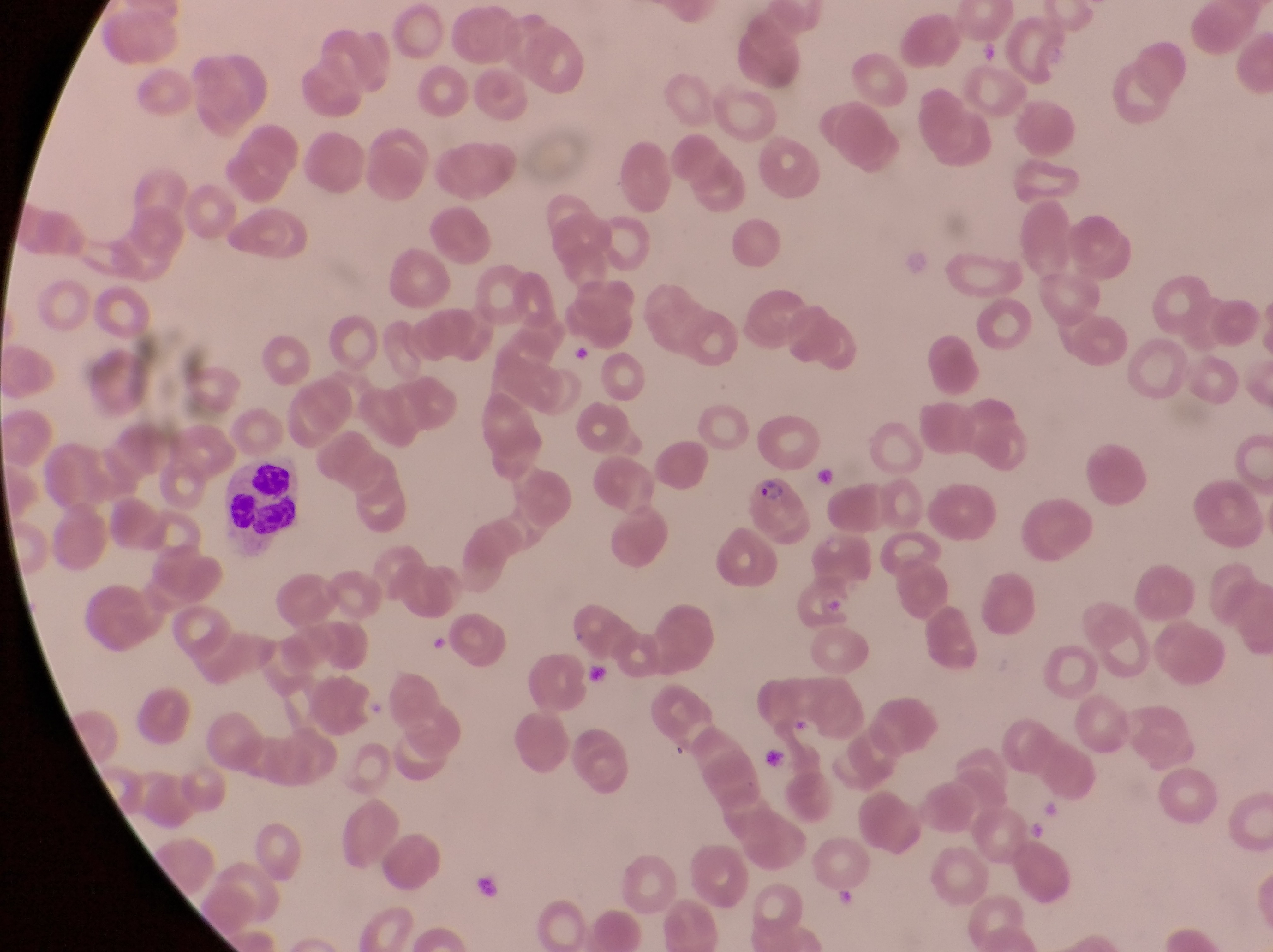 Approximate bounding boxes as left top right bottom in pixels. Leukocyte locations: 222 467 319 550. Parasitised red blood cell locations: 747 474 819 552. Artifact (platelet-like body, stain precipitate, or debris) locations: 567 344 597 374; 430 628 453 654; 586 665 617 691; 756 742 793 787; 477 877 506 905. Collected in Uganda. Thin blood smear. Image is 1273×952 pixels. One field of view. Photographed through the eyepiece of an Olympus CX-23 microscope with a smartphone camera. Magnification of 1000x.